Report the malaria status.
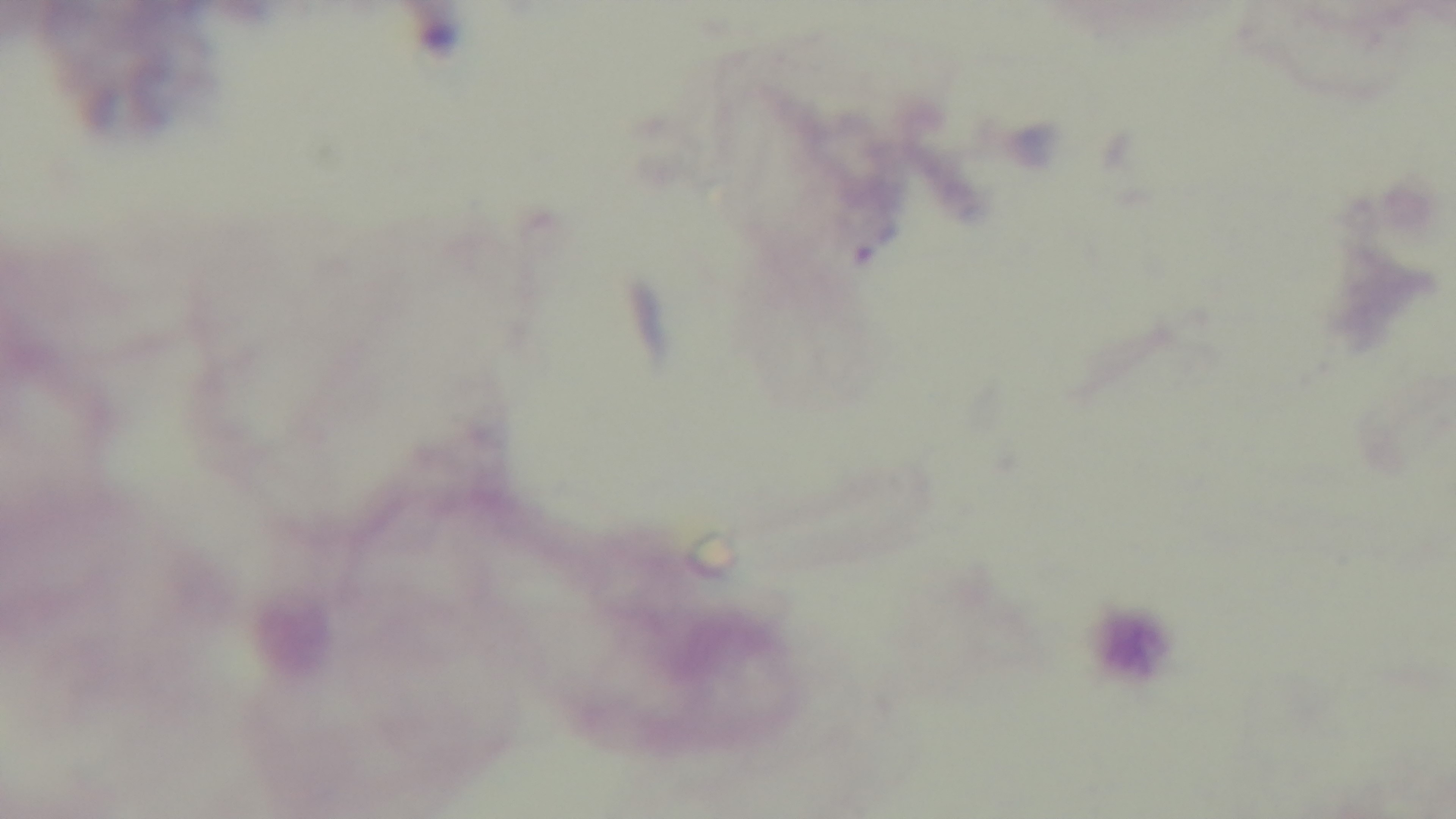
It is uninfected.

Summary:
  - Modality: light microscopy
  - Stain: Giemsa
  - Field of view: single
  - Objective: 100x oil immersion
  - Preparation: thick smear
  - Capture: mounted 4K digital camera